State which parasite is depicted.
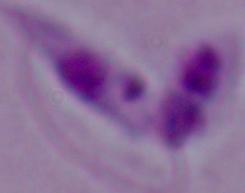

This is Leishmania.

modality = micrograph
magnification = 1000x